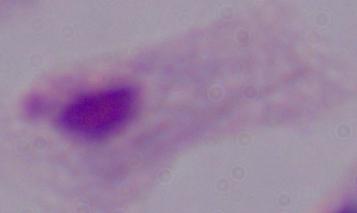
magnification = 1000x
identification = trichomonad
modality = micrograph